Locate every Plasmodium parasite.
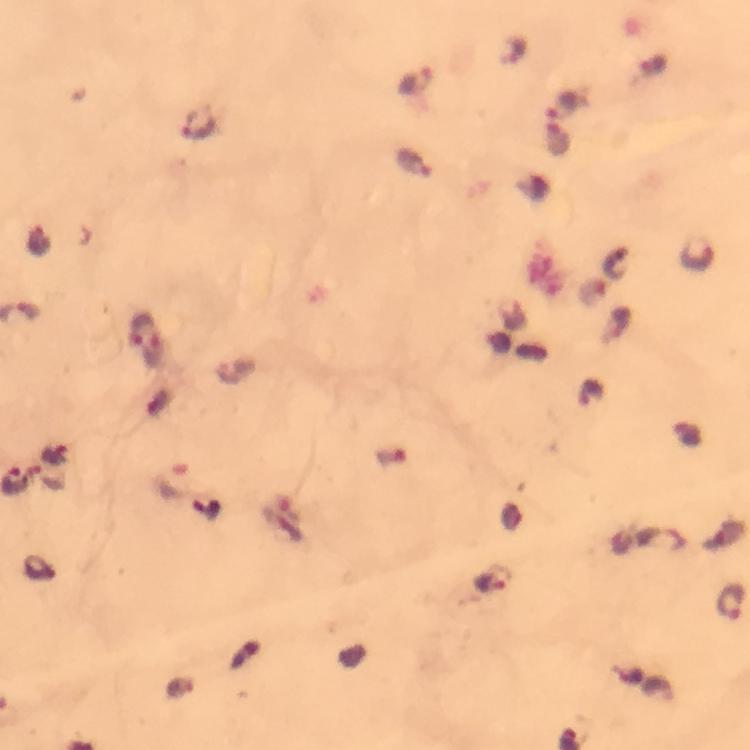
Approximate centers as (x, y) in pixels.
Plasmodium parasites: (416, 80), (564, 105), (202, 122), (556, 139), (414, 163), (39, 239), (697, 254), (592, 293), (138, 327), (154, 350), (492, 580), (730, 603).

Photographed with a smartphone mounted on the microscope. A crop from one field of view. Image is 750×750 pixels. From a malaria diagnostic workup. Giemsa stain. Immersion oil was used. At 100x magnification. Thick blood smear.